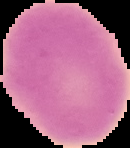 From a thin blood smear. The area outside the segmented cell region is set to black. Result: negative for malaria parasites. Image is 130×148 pixels.